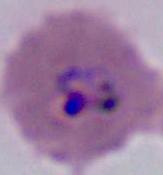
Summary:
  - Identification: Plasmodium
  - Modality: photomicrograph
  - Magnification: 400x or 1000x